Assess for malaria.
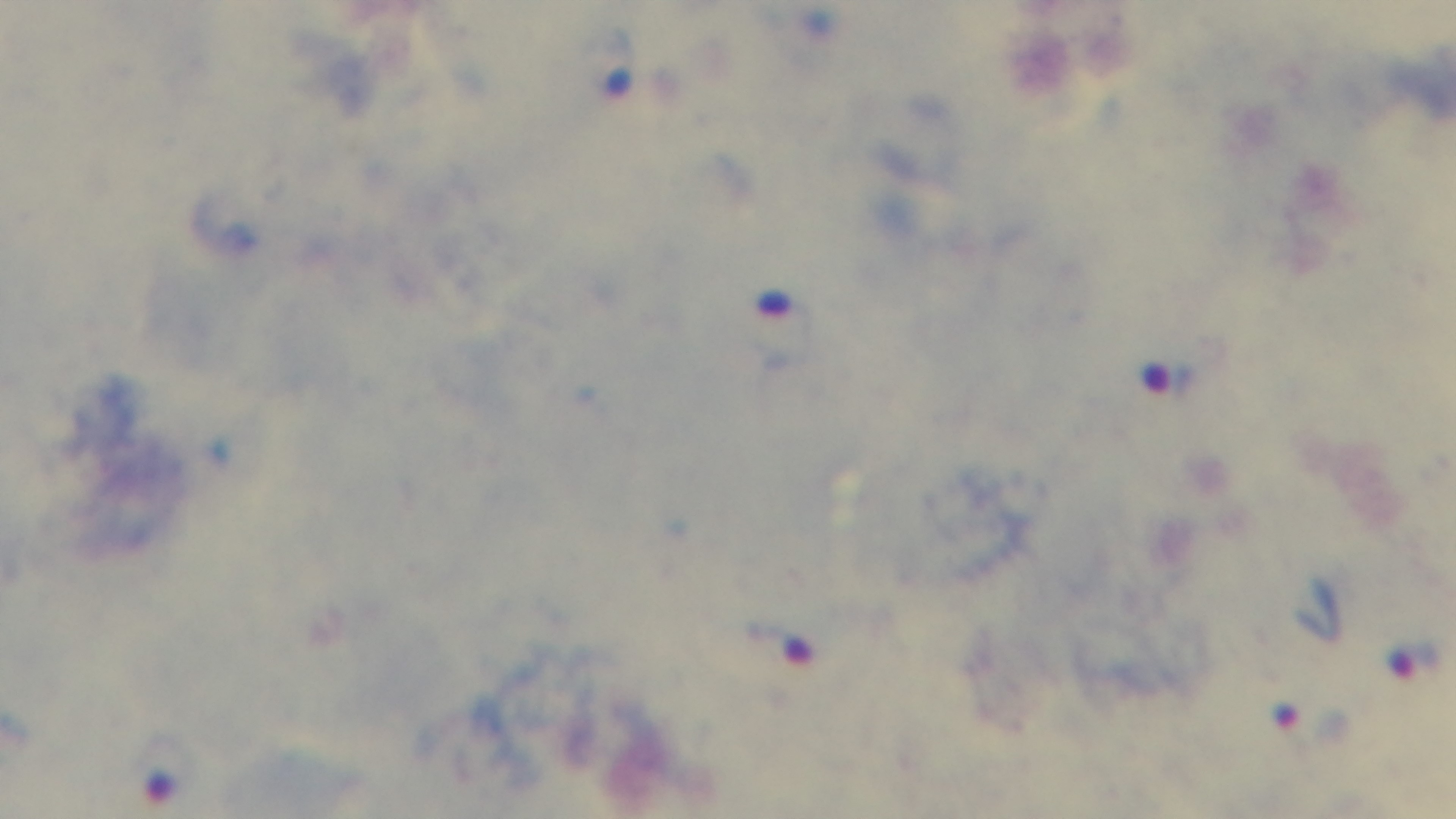
Positive.

Summary:
  - Objective: 100x oil immersion
  - Capture: mounted 4K digital camera
  - Modality: light microscopy
  - Stain: Giemsa
  - Field of view: one from the slide
  - Preparation: thick blood film